State which parasite is depicted.
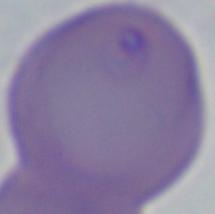

This is Babesia.

Captured at 1000x magnification. Photomicrograph.